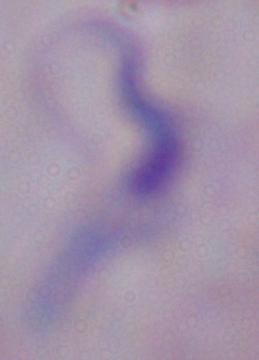
Summary:
  - Magnification: 1000x
  - Modality: photomicrograph
  - Identification: trypanosome